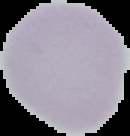

Summary:
  - Image type: cell region segmented out of the field of view; surrounding area masked to black
  - Result: no malaria parasites detected
  - Preparation: thin blood film
  - Image size: 130×136 pixels